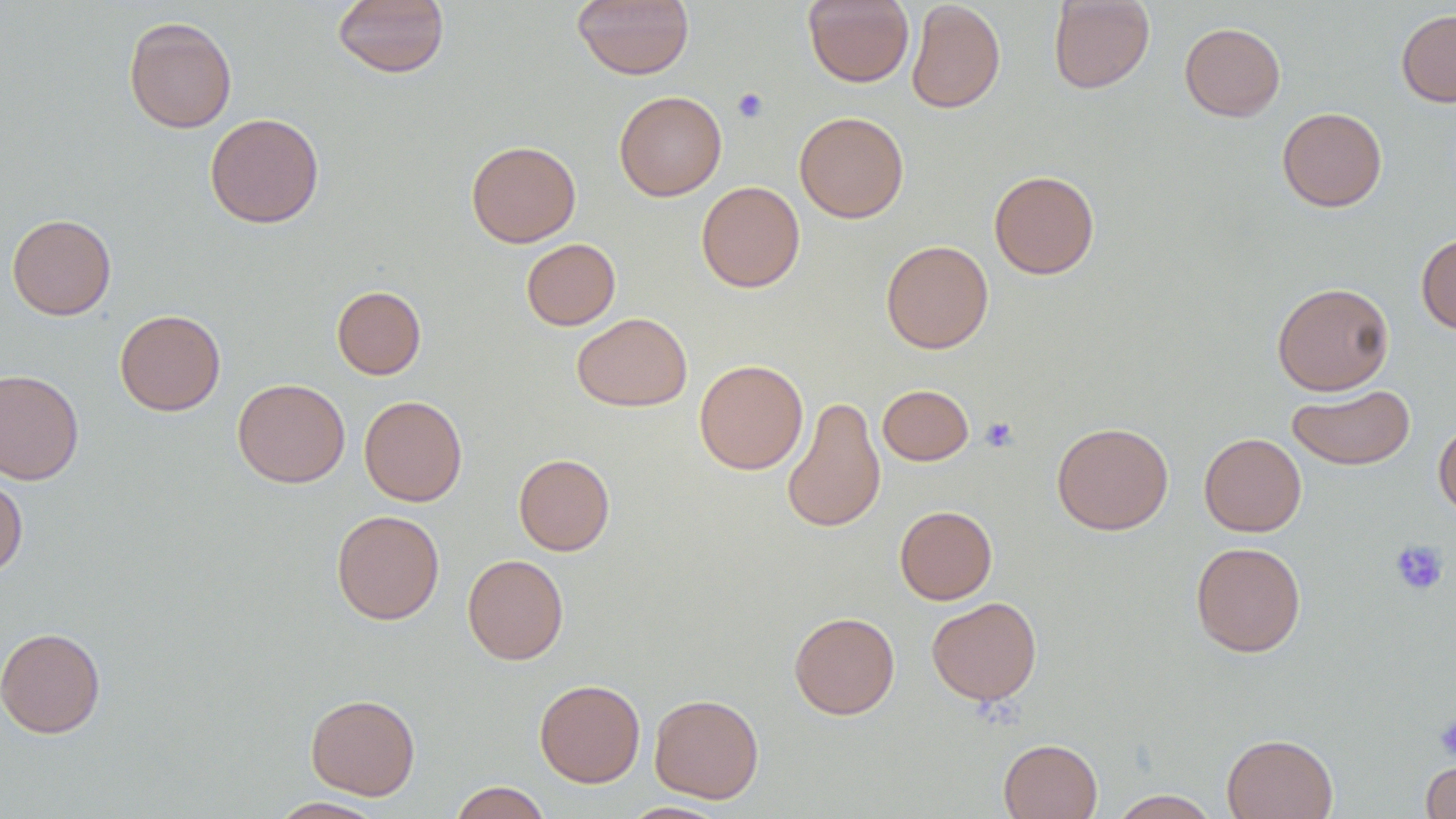
Approximate bounding boxes as [x1, y1, x2, y2] in pixels. Platelet locations: [732, 87, 769, 122], [980, 416, 1019, 452], [1390, 539, 1449, 595], [1433, 714, 1456, 761]. Uninfected red blood cell locations: [332, 0, 450, 78], [803, 0, 914, 88], [906, 0, 1005, 113], [1048, 0, 1155, 94], [572, 1, 693, 80], [1396, 8, 1456, 107], [123, 16, 237, 133], [1180, 22, 1285, 121], [613, 90, 727, 201], [1277, 107, 1387, 212], [794, 111, 909, 223], [204, 113, 325, 228], [466, 140, 581, 247], [989, 170, 1100, 279], [696, 181, 805, 293], [7, 213, 116, 320], [1416, 231, 1456, 335], [521, 238, 620, 330], [881, 240, 994, 353], [1271, 282, 1395, 395], [331, 286, 426, 379], [114, 310, 226, 416], [572, 312, 692, 411], [694, 359, 808, 475], [0, 368, 84, 485], [232, 378, 350, 488], [878, 384, 973, 465], [1287, 385, 1414, 470], [359, 395, 467, 506], [782, 396, 886, 534], [1434, 420, 1456, 518], [1052, 421, 1174, 535], [1199, 433, 1306, 536], [513, 453, 615, 555], [0, 476, 28, 578], [895, 505, 997, 604], [331, 509, 445, 625], [1190, 541, 1306, 657], [462, 554, 568, 665], [926, 596, 1042, 705], [788, 611, 900, 719], [0, 626, 106, 738], [534, 679, 645, 787], [305, 693, 420, 800], [649, 694, 764, 803], [1222, 733, 1338, 819], [998, 738, 1103, 819], [1422, 759, 1456, 818], [450, 781, 551, 819], [1109, 789, 1221, 818], [269, 797, 388, 818], [620, 801, 731, 818]. Slide-level diagnosis: negative for blood parasites. Optical microscopy. Image is 1456×819 pixels. Thin blood smear. One field of a larger specimen. Captured at 1000x magnification.